Locate every blood parasite and identify its species.
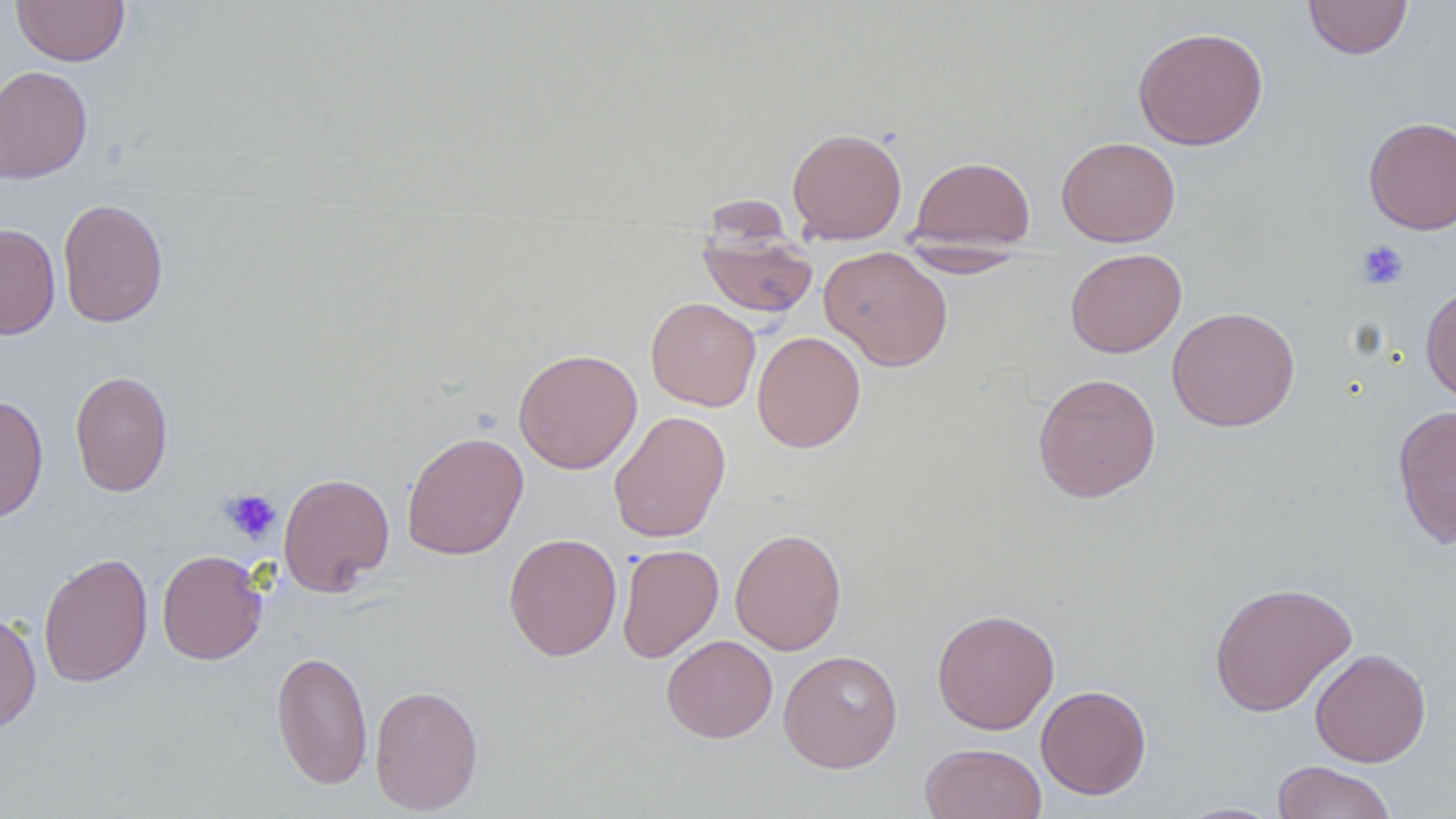
No blood parasites seen.

Summary:
  - Coordinate format: approximate bounding boxes as named x1/y1/x2/y2 corners in pixels
  - Uninfected red blood cell locations: (x1=10, y1=0, x2=130, y2=66), (x1=1303, y1=0, x2=1413, y2=60), (x1=1132, y1=26, x2=1269, y2=151), (x1=0, y1=65, x2=92, y2=184), (x1=1363, y1=116, x2=1456, y2=235), (x1=787, y1=126, x2=907, y2=244), (x1=1056, y1=136, x2=1181, y2=246), (x1=908, y1=156, x2=1035, y2=252), (x1=57, y1=197, x2=168, y2=328), (x1=0, y1=224, x2=60, y2=340), (x1=696, y1=230, x2=818, y2=319), (x1=897, y1=244, x2=1030, y2=278), (x1=818, y1=245, x2=954, y2=371), (x1=1065, y1=248, x2=1186, y2=358), (x1=1421, y1=283, x2=1456, y2=403), (x1=645, y1=297, x2=761, y2=412), (x1=1166, y1=306, x2=1301, y2=432), (x1=752, y1=330, x2=866, y2=453), (x1=513, y1=348, x2=642, y2=474), (x1=70, y1=370, x2=172, y2=497), (x1=1032, y1=372, x2=1161, y2=503), (x1=0, y1=394, x2=48, y2=523), (x1=1393, y1=404, x2=1456, y2=548), (x1=608, y1=410, x2=731, y2=543), (x1=401, y1=431, x2=529, y2=560), (x1=277, y1=472, x2=395, y2=597), (x1=730, y1=528, x2=847, y2=655), (x1=503, y1=533, x2=622, y2=661), (x1=617, y1=543, x2=724, y2=662), (x1=157, y1=550, x2=268, y2=665), (x1=38, y1=552, x2=154, y2=688), (x1=1208, y1=580, x2=1358, y2=717), (x1=931, y1=608, x2=1060, y2=734), (x1=0, y1=610, x2=42, y2=735), (x1=662, y1=635, x2=777, y2=743), (x1=1309, y1=648, x2=1431, y2=767), (x1=271, y1=649, x2=373, y2=789), (x1=778, y1=650, x2=903, y2=772), (x1=369, y1=684, x2=484, y2=815), (x1=1035, y1=684, x2=1152, y2=799), (x1=919, y1=742, x2=1047, y2=819), (x1=1271, y1=761, x2=1398, y2=819), (x1=1177, y1=802, x2=1285, y2=818)
  - Platelet locations: (x1=1356, y1=240, x2=1409, y2=290), (x1=220, y1=489, x2=282, y2=544)
  - Slide-level diagnosis: no evidence of blood parasites
  - Modality: light microscopy
  - Image size: 1456×819 pixels
  - Stain: May-Grünwald-Giemsa
  - Magnification: 1000x
  - Preparation: thin blood film
  - Field of view: single